Locate every blood parasite and identify its species.
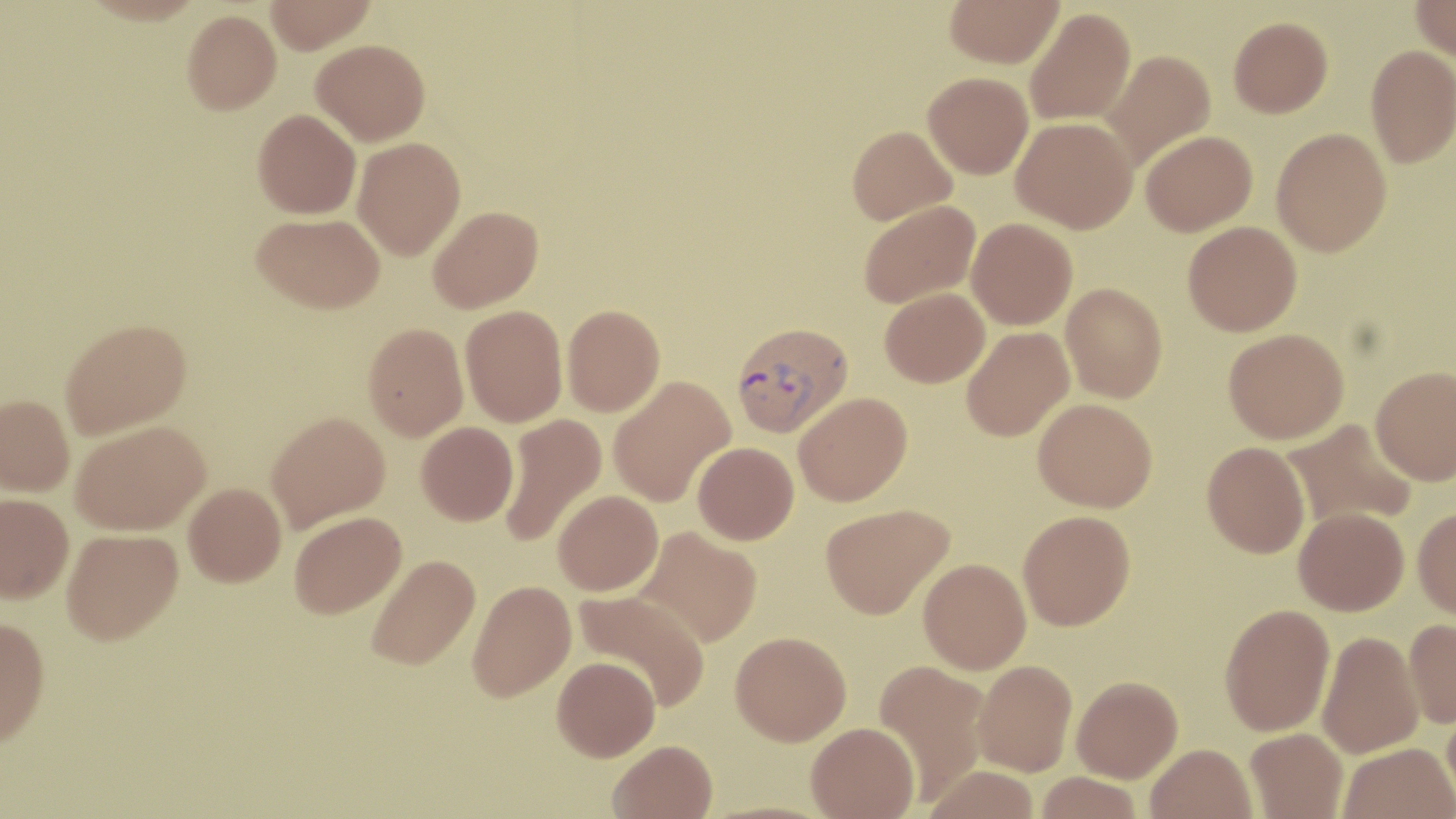
Approximate bounding boxes as (x1, y1, x2, y2) in pixels.
Plasmodium vivax-infected red blood cells: (731, 321, 853, 438).
No Plasmodium falciparum, Plasmodium ovale, Plasmodium malariae, Babesia divergens, or Trypanosoma brucei observed.

slide-level diagnosis = Plasmodium vivax
uninfected red blood cell locations = approximate bounding boxes as (x1, y1, x2, y2) in pixels: (265, 0, 376, 54), (944, 0, 1064, 68), (1410, 0, 1456, 62), (1025, 7, 1136, 126), (182, 9, 281, 115), (1229, 16, 1333, 117), (311, 39, 430, 144), (1366, 45, 1456, 166), (1099, 49, 1216, 170), (923, 72, 1034, 178), (253, 108, 361, 219), (1011, 117, 1137, 233), (847, 125, 957, 224), (1271, 127, 1392, 256), (1140, 130, 1258, 235), (352, 137, 466, 260), (859, 200, 980, 308), (428, 205, 543, 312), (253, 212, 384, 313), (967, 218, 1078, 330), (1183, 221, 1302, 335), (1061, 282, 1167, 402), (880, 287, 989, 387), (460, 305, 567, 426), (562, 305, 665, 416), (60, 318, 192, 438), (363, 323, 468, 440), (962, 327, 1074, 442), (1223, 328, 1349, 443), (1371, 365, 1456, 485), (607, 375, 735, 507), (793, 392, 912, 506), (0, 394, 75, 495), (1033, 398, 1157, 512), (266, 411, 390, 532), (500, 413, 607, 546), (1283, 418, 1418, 531), (71, 420, 210, 535), (417, 421, 518, 525), (1202, 441, 1310, 557), (693, 442, 799, 544), (184, 482, 286, 586), (554, 490, 663, 595), (1, 493, 74, 602), (820, 503, 953, 619), (1294, 506, 1409, 615), (1413, 507, 1456, 620), (1018, 510, 1135, 630), (289, 511, 406, 618), (636, 526, 762, 647), (62, 528, 183, 646), (365, 554, 480, 671), (919, 558, 1031, 674), (467, 580, 576, 701), (573, 588, 710, 710), (1220, 603, 1335, 736), (0, 617, 50, 751), (1404, 618, 1456, 728), (731, 631, 851, 745), (1317, 631, 1423, 758), (552, 656, 661, 761), (873, 660, 991, 801), (973, 660, 1077, 776), (1072, 675, 1183, 782), (1442, 701, 1456, 812), (806, 722, 920, 819), (1245, 728, 1347, 819), (607, 740, 718, 819), (1338, 742, 1455, 819), (1146, 743, 1257, 819), (923, 764, 1040, 819), (1036, 772, 1142, 818)
preparation = thin blood film
image size = 1456×819 pixels
modality = light microscopy
magnification = 1000x
stain = May-Grünwald-Giemsa
field of view = one of a larger specimen